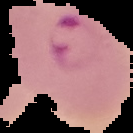 Malaria status: parasitized. Image is 133×133 pixels. From a thin blood film. The area outside the segmented cell region is set to black.